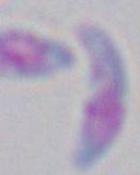

modality = micrograph
magnification = 1000x
identification = Toxoplasma gondii